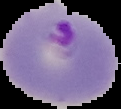

malaria status = parasitized
image size = 121×109 pixels
image type = segmented cell region with the area outside set to black
preparation = thin blood smear